Give the position of every leukocyte visible.
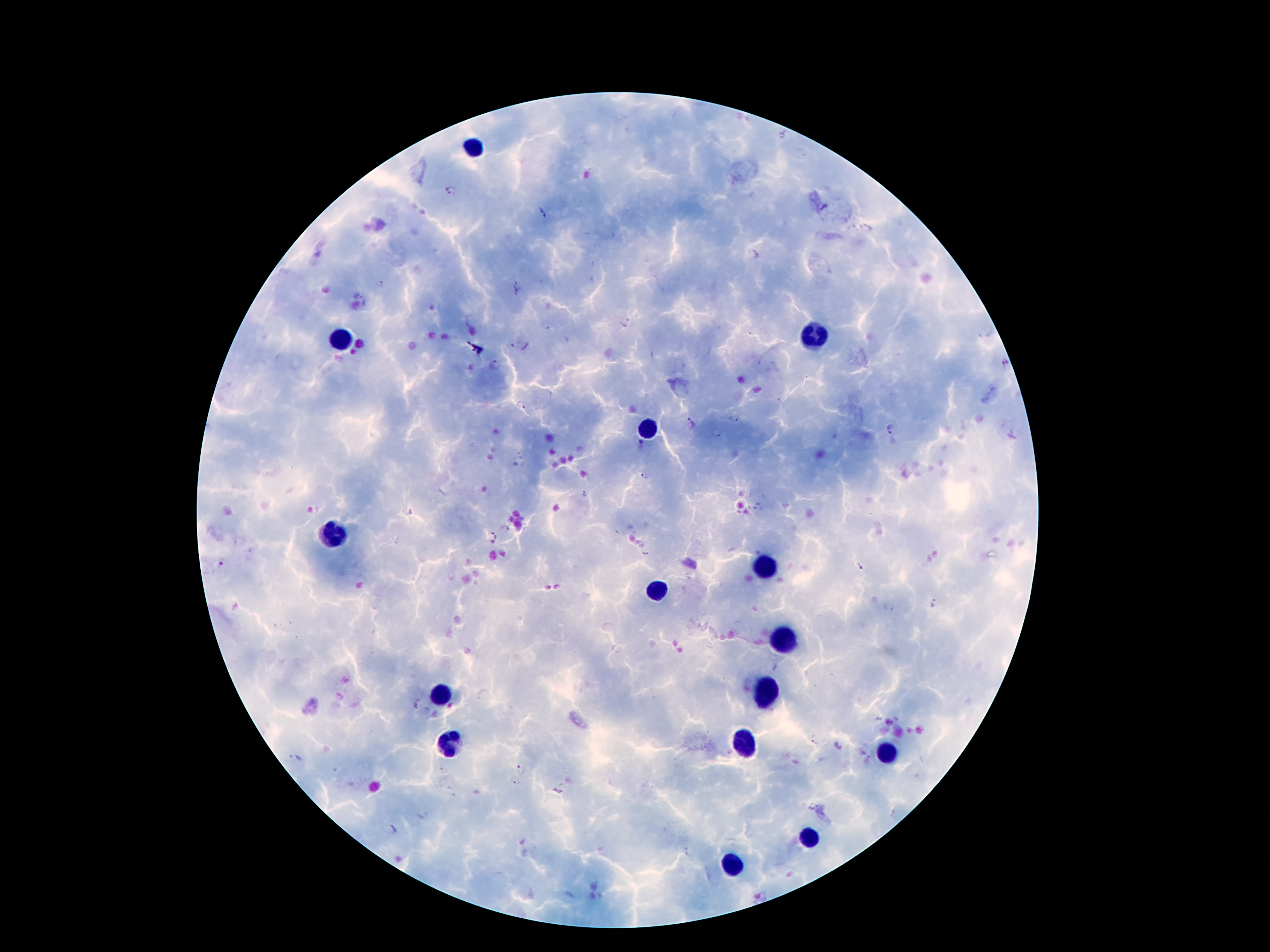
Approximate centers as {x, y} in pixels.
Leukocytes: {474, 149}, {814, 336}, {339, 342}, {648, 431}, {333, 535}, {760, 567}, {655, 590}, {781, 637}, {764, 692}, {440, 696}, {745, 742}, {447, 747}, {886, 752}, {808, 835}, {730, 866}.

Plasmodium parasite locations = {450, 191}, {541, 214}, {383, 284}, {517, 288}, {546, 325}, {519, 346}, {1003, 362}, {497, 363}, {520, 405}, {732, 419}, {692, 421}, {892, 429}, {715, 433}, {522, 462}, {645, 477}, {583, 494}, {760, 507}, {410, 513}, {492, 535}, {644, 555}, {219, 564}, {859, 565}, {935, 602}, {815, 741}, {296, 758}, {523, 768}, {514, 781}, {813, 806}, {391, 830}, {687, 853}
field of view = one from this slide
preparation = thick blood film
image size = 1270×952 pixels
magnification = 100x
patient malaria status = infected with Plasmodium falciparum
capture = smartphone through the microscope eyepiece
stain = Giemsa